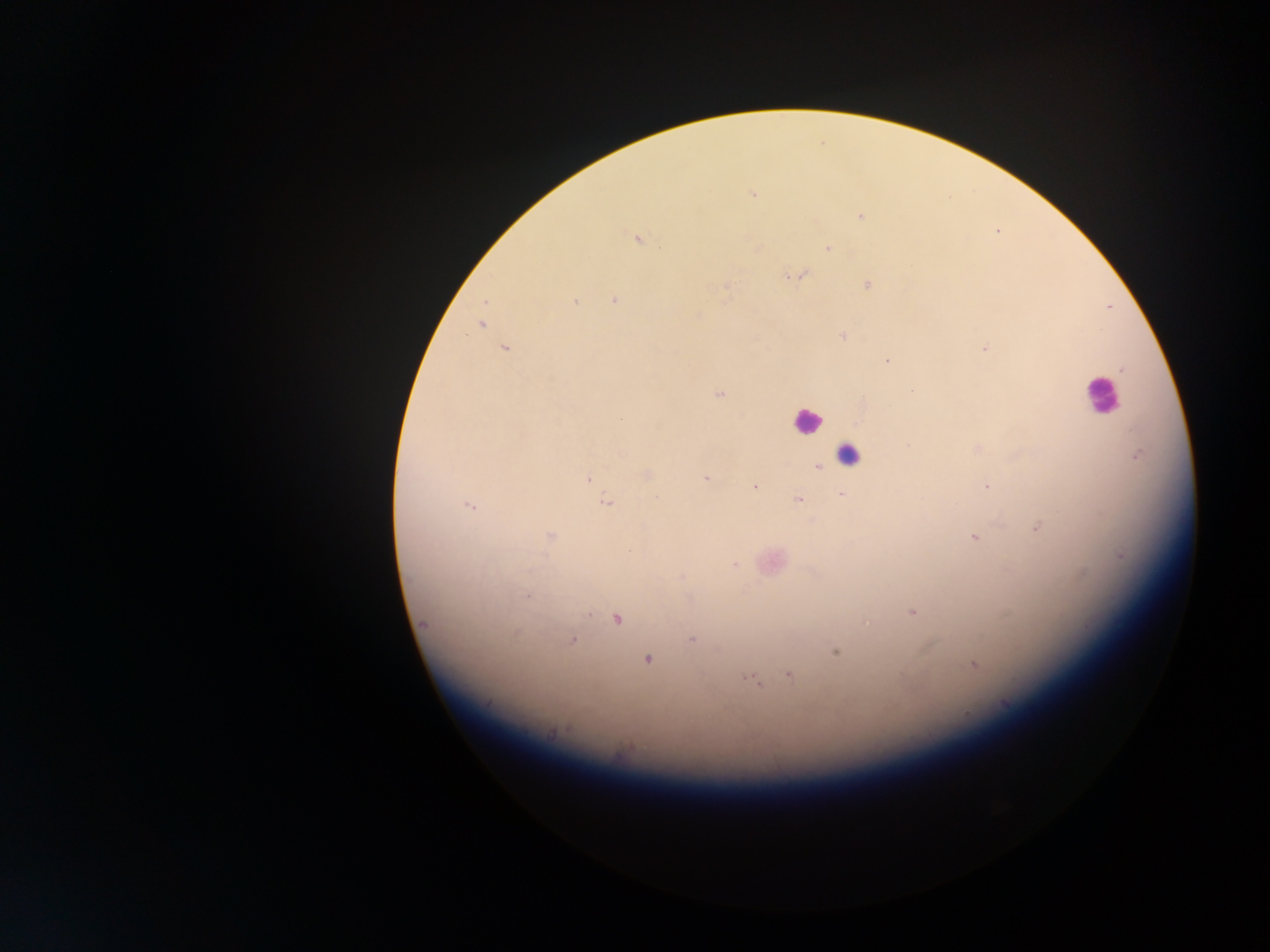

malaria parasite locations = approximate centers as {x, y} in pixels: {753, 193}, {860, 216}, {637, 240}, {828, 248}, {797, 276}, {868, 285}, {726, 286}, {574, 301}, {614, 301}, {486, 302}, {481, 325}, {843, 336}, {504, 349}, {984, 349}, {887, 361}, {1122, 370}, {718, 394}, {620, 420}, {908, 445}, {623, 454}, {1137, 456}, {818, 467}, {647, 475}, {589, 478}, {706, 478}, {986, 485}, {755, 486}, {842, 494}, {656, 497}, {798, 500}, {605, 502}, {470, 506}, {1038, 527}, {550, 536}, {974, 538}, {734, 564}, {681, 578}, {526, 596}, {912, 612}, {617, 620}, {867, 622}, {424, 624}, {691, 639}, {572, 641}, {835, 652}, {647, 659}, {974, 666}, {789, 675}, {752, 680}, {1005, 705}, {552, 733}
leukocyte locations = approximate centers as {x, y} in pixels: {1100, 394}, {807, 420}, {847, 454}
image size = 1270×952 pixels
country = Ghana
capture = mobile-phone photograph through a microscope
field of view = single
preparation = thick blood film